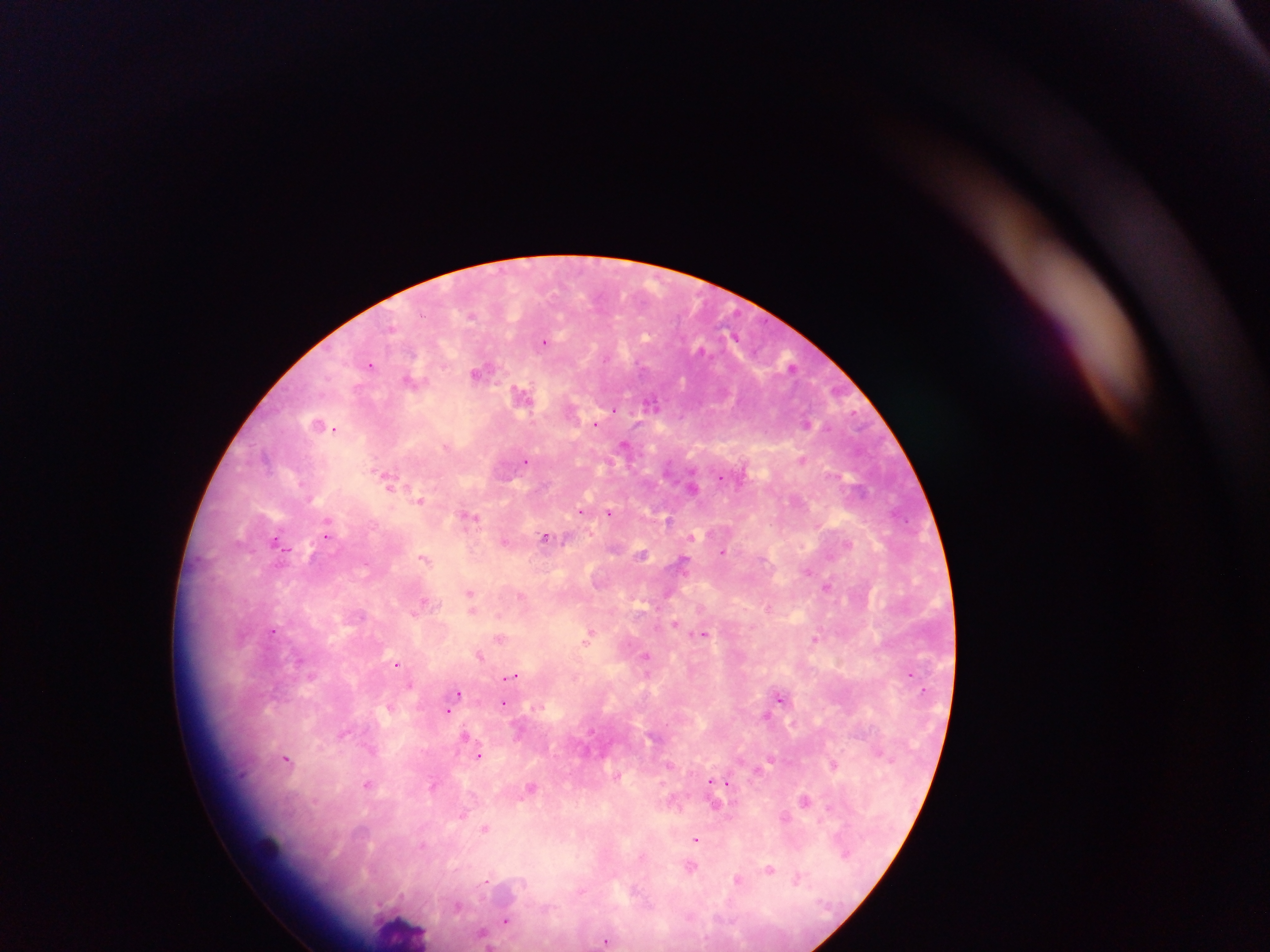
country = Ghana
field of view = single
capture = mobile-phone photograph through a microscope
Plasmodium parasite locations = approximate centers as [x, y] in pixels: [472, 315], [545, 342], [370, 365], [792, 366], [480, 372], [411, 380], [523, 394], [652, 403], [614, 409], [807, 423], [597, 424], [318, 425], [336, 429], [624, 445], [526, 460], [802, 460], [720, 477], [387, 478], [692, 486], [420, 499], [580, 511], [609, 513], [469, 516], [669, 520], [327, 523], [327, 533], [545, 537], [692, 537], [277, 541], [505, 541], [848, 545], [723, 552], [642, 554], [424, 557], [683, 562], [807, 571], [827, 586], [667, 593], [470, 595], [522, 596], [425, 602], [471, 604], [769, 607], [360, 615], [675, 623], [272, 630], [704, 634], [588, 637], [501, 638], [815, 639], [479, 655], [646, 657], [397, 664], [513, 675], [458, 694], [780, 696], [504, 703], [389, 707], [448, 710], [767, 715], [342, 735], [465, 735], [479, 755], [287, 759], [833, 765], [368, 783], [433, 783], [711, 783], [727, 783], [530, 787], [805, 799], [716, 805], [829, 807], [462, 814], [785, 817], [484, 829], [696, 840], [845, 854], [691, 868], [770, 868], [738, 878], [797, 879], [635, 890], [457, 906], [506, 920], [483, 934], [605, 941]
image size = 1270×952 pixels
preparation = thick blood smear
leukocyte locations = approximate centers as [x, y] in pixels: [264, 849], [402, 931]